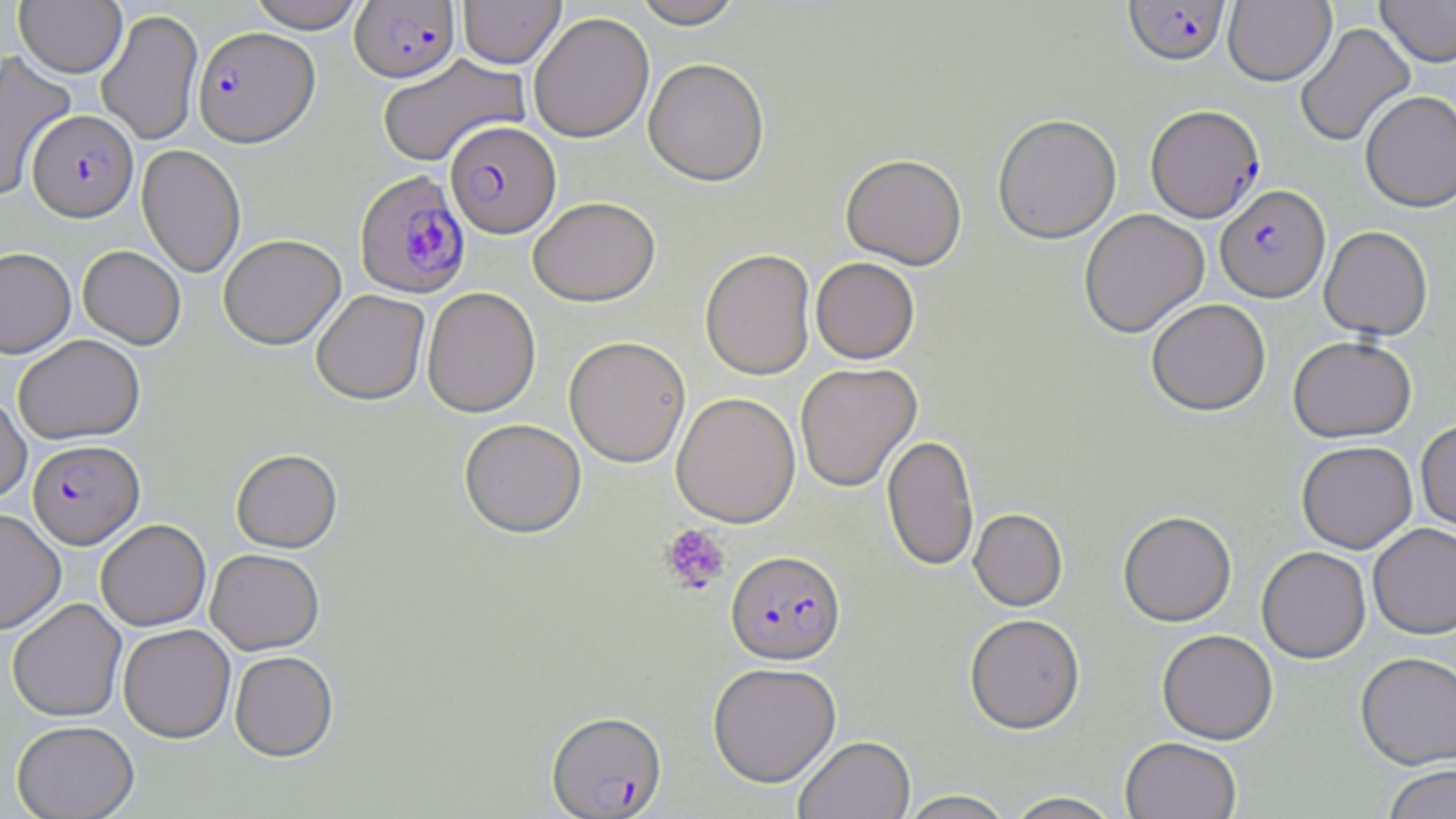

Summary:
  - Coordinate format: approximate bounding boxes as (x1, y1, x2, y2) in pixels
  - Plasmodium falciparum-infected red blood cell locations: (1123, 0, 1231, 68), (350, 1, 460, 83), (193, 27, 319, 147), (1145, 105, 1265, 223), (27, 110, 138, 222), (445, 122, 561, 239), (355, 171, 471, 300), (1215, 185, 1330, 303), (27, 440, 144, 549), (726, 552, 846, 666), (546, 711, 668, 818)
  - Platelet locations: (660, 523, 730, 594)
  - Uninfected red blood cell locations: (246, 0, 367, 33), (458, 0, 565, 70), (633, 0, 745, 31), (1224, 0, 1335, 86), (1376, 0, 1456, 67), (14, 1, 126, 77), (96, 8, 203, 146), (529, 13, 654, 145), (1295, 21, 1416, 148), (0, 51, 77, 202), (377, 54, 531, 168), (643, 60, 769, 189), (1359, 90, 1456, 212), (993, 115, 1121, 246), (136, 145, 246, 278), (841, 157, 966, 271), (528, 199, 661, 308), (1079, 209, 1209, 338), (1319, 226, 1433, 341), (219, 235, 346, 350), (78, 246, 186, 349), (0, 248, 76, 358), (700, 251, 816, 382), (810, 258, 920, 365), (422, 287, 541, 418), (311, 290, 430, 407), (1146, 299, 1271, 416), (14, 334, 145, 444), (1288, 336, 1417, 442), (564, 337, 690, 469), (795, 363, 922, 493), (0, 392, 32, 505), (671, 393, 801, 529), (1415, 419, 1456, 536), (459, 420, 586, 540), (882, 434, 979, 572), (1296, 441, 1417, 553), (231, 449, 342, 554), (0, 508, 66, 635), (969, 509, 1068, 612), (1118, 511, 1236, 627), (96, 519, 211, 631), (1368, 522, 1456, 639), (1256, 546, 1371, 663), (205, 548, 324, 655), (7, 598, 127, 721), (964, 614, 1085, 734), (118, 624, 235, 743), (1157, 630, 1278, 745), (229, 651, 338, 762), (1355, 651, 1456, 770), (708, 663, 841, 788), (11, 720, 139, 819), (793, 735, 915, 819), (1120, 737, 1242, 819), (1382, 764, 1456, 819), (897, 790, 1016, 819), (1003, 791, 1123, 819)
  - Slide-level diagnosis: Plasmodium falciparum
  - Modality: optical microscopy
  - Image size: 1456×819 pixels
  - Preparation: thin blood smear
  - Magnification: 1000x
  - Stain: May-Grünwald-Giemsa
  - Field of view: single